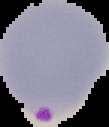 Image is 109×127 pixels. Result: Plasmodium parasites identified. Segmented cell region on a black background. From a thin blood film.